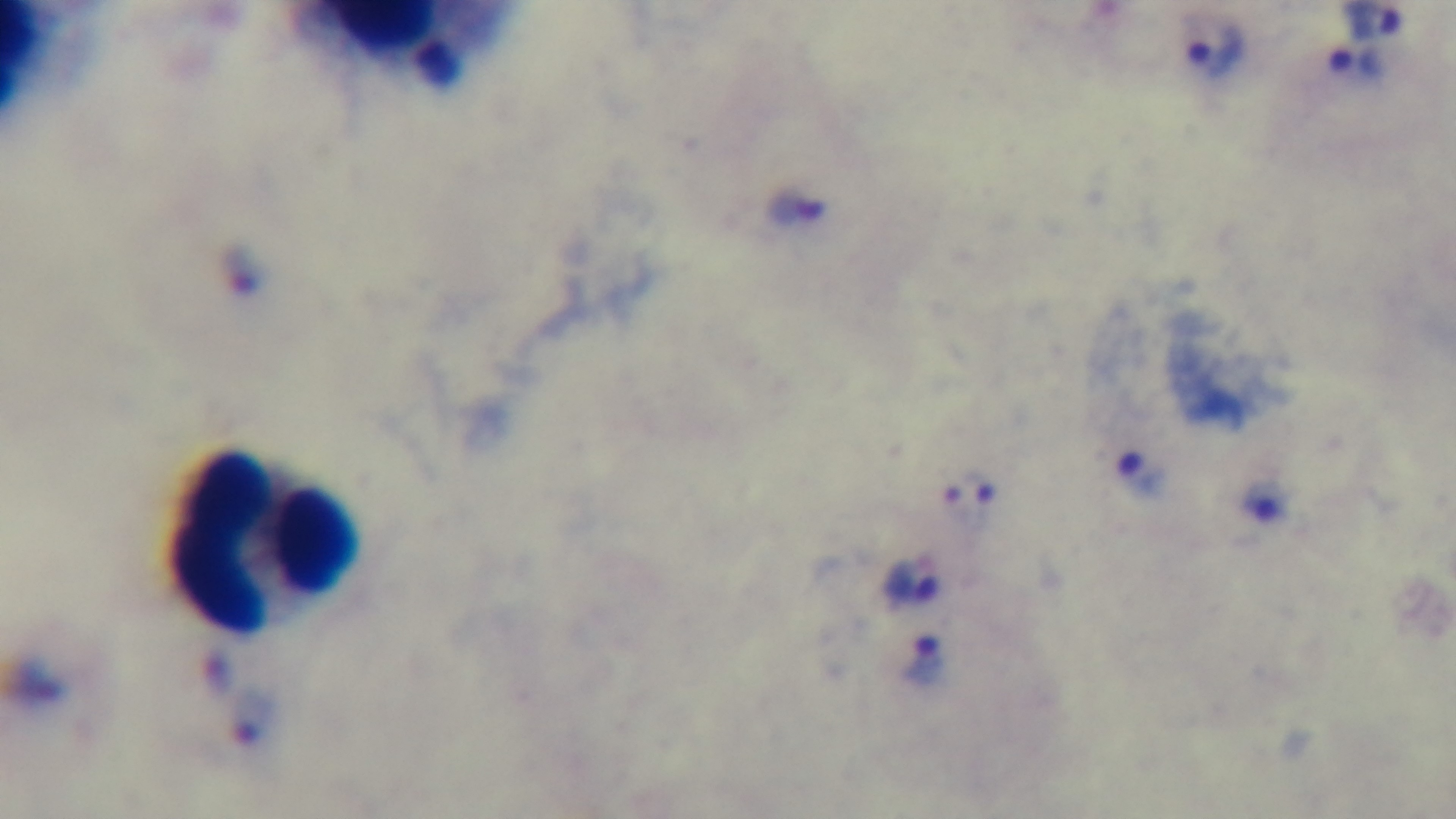
{
  "capture": "mounted 4K digital camera",
  "modality": "light microscopy",
  "field_of_view": "one from the slide",
  "preparation": "thick",
  "objective": "100x oil immersion",
  "stain": "Giemsa",
  "malaria_status": "positive"
}